Name the cell type shown.
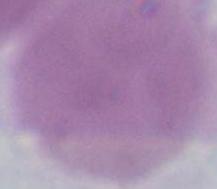
An erythrocyte.

Summary:
  - Magnification: 1000x
  - Modality: micrograph